Name the parasite shown.
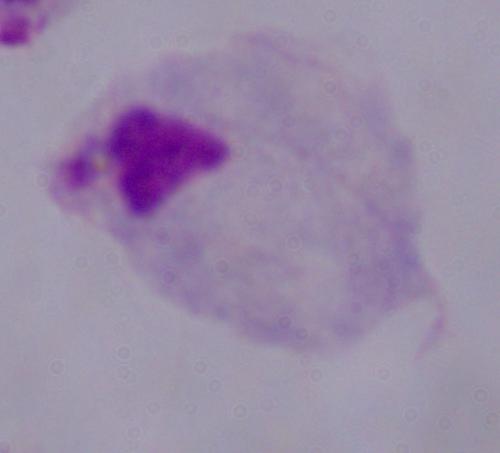
A trichomonad.

Summary:
  - Magnification: 1000x
  - Modality: micrograph